State which parasite is depicted.
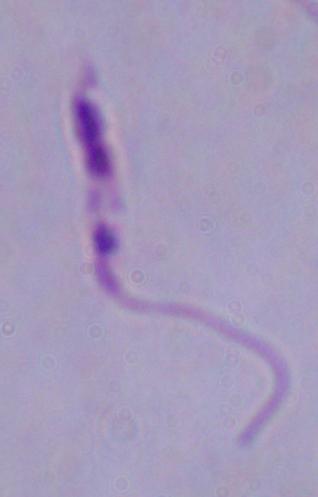
This is Leishmania.

modality = photomicrograph
magnification = 1000x